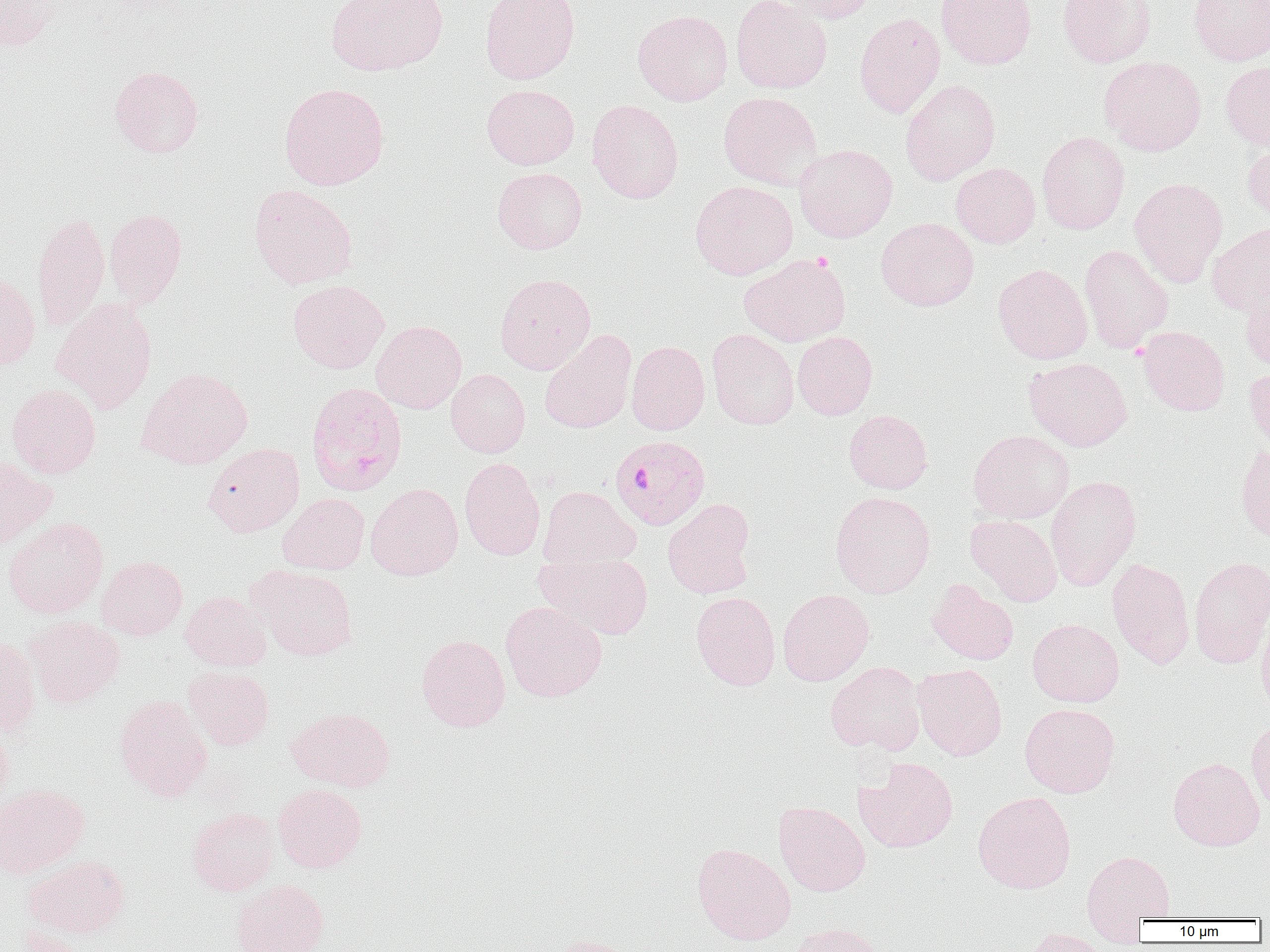 Approximate bounding boxes as named x1/y1/x2/y2 corners in pixels. Uninfected red blood cell locations: (x1=0, y1=0, x2=59, y2=51), (x1=325, y1=0, x2=448, y2=76), (x1=480, y1=0, x2=581, y2=85), (x1=731, y1=0, x2=832, y2=93), (x1=776, y1=0, x2=880, y2=23), (x1=936, y1=0, x2=1038, y2=69), (x1=1058, y1=0, x2=1156, y2=68), (x1=1188, y1=0, x2=1269, y2=66), (x1=633, y1=9, x2=733, y2=106), (x1=853, y1=12, x2=945, y2=118), (x1=1099, y1=56, x2=1207, y2=156), (x1=1221, y1=60, x2=1270, y2=152), (x1=109, y1=65, x2=204, y2=158), (x1=900, y1=80, x2=1001, y2=185), (x1=279, y1=82, x2=389, y2=190), (x1=481, y1=84, x2=579, y2=169), (x1=718, y1=92, x2=823, y2=191), (x1=587, y1=100, x2=683, y2=203), (x1=1037, y1=131, x2=1130, y2=234), (x1=1242, y1=139, x2=1270, y2=223), (x1=794, y1=144, x2=898, y2=242), (x1=950, y1=163, x2=1040, y2=248), (x1=492, y1=167, x2=587, y2=254), (x1=1129, y1=177, x2=1228, y2=287), (x1=690, y1=180, x2=798, y2=280), (x1=248, y1=184, x2=358, y2=290), (x1=104, y1=208, x2=187, y2=306), (x1=32, y1=213, x2=110, y2=331), (x1=876, y1=217, x2=979, y2=311), (x1=1207, y1=222, x2=1270, y2=318), (x1=1079, y1=244, x2=1173, y2=354), (x1=739, y1=254, x2=851, y2=347), (x1=992, y1=264, x2=1092, y2=364), (x1=0, y1=271, x2=40, y2=370), (x1=495, y1=273, x2=596, y2=374), (x1=287, y1=280, x2=389, y2=373), (x1=1240, y1=286, x2=1270, y2=373), (x1=52, y1=299, x2=157, y2=414), (x1=371, y1=321, x2=467, y2=414), (x1=1137, y1=326, x2=1230, y2=415), (x1=707, y1=328, x2=799, y2=430), (x1=539, y1=330, x2=637, y2=433), (x1=792, y1=331, x2=878, y2=420), (x1=626, y1=341, x2=710, y2=435), (x1=1024, y1=357, x2=1132, y2=451), (x1=1244, y1=363, x2=1270, y2=456), (x1=137, y1=367, x2=252, y2=469), (x1=446, y1=369, x2=531, y2=458), (x1=6, y1=383, x2=101, y2=478), (x1=843, y1=410, x2=933, y2=493), (x1=968, y1=430, x2=1074, y2=524), (x1=202, y1=443, x2=304, y2=537), (x1=1235, y1=443, x2=1270, y2=545), (x1=0, y1=455, x2=57, y2=550), (x1=459, y1=457, x2=546, y2=560), (x1=1045, y1=475, x2=1142, y2=592), (x1=366, y1=483, x2=463, y2=581), (x1=537, y1=485, x2=641, y2=570), (x1=830, y1=490, x2=935, y2=598), (x1=278, y1=493, x2=369, y2=574), (x1=663, y1=499, x2=757, y2=599), (x1=965, y1=514, x2=1062, y2=606), (x1=3, y1=517, x2=108, y2=618), (x1=536, y1=551, x2=653, y2=640), (x1=96, y1=556, x2=187, y2=641), (x1=1189, y1=556, x2=1270, y2=669), (x1=1107, y1=558, x2=1195, y2=669), (x1=250, y1=565, x2=358, y2=661), (x1=927, y1=579, x2=1019, y2=665), (x1=777, y1=589, x2=875, y2=686), (x1=180, y1=591, x2=271, y2=672), (x1=691, y1=591, x2=780, y2=691), (x1=500, y1=601, x2=607, y2=702), (x1=1256, y1=612, x2=1270, y2=717), (x1=24, y1=616, x2=124, y2=709), (x1=1027, y1=619, x2=1124, y2=707), (x1=417, y1=634, x2=510, y2=731), (x1=0, y1=637, x2=41, y2=736), (x1=825, y1=661, x2=926, y2=755), (x1=912, y1=663, x2=1007, y2=760), (x1=183, y1=666, x2=274, y2=750), (x1=113, y1=695, x2=212, y2=801), (x1=1020, y1=703, x2=1120, y2=798), (x1=286, y1=707, x2=395, y2=791), (x1=1246, y1=716, x2=1270, y2=816), (x1=0, y1=721, x2=13, y2=810), (x1=854, y1=757, x2=958, y2=854), (x1=1168, y1=757, x2=1265, y2=851), (x1=273, y1=783, x2=366, y2=872), (x1=0, y1=784, x2=88, y2=878), (x1=972, y1=791, x2=1076, y2=894), (x1=773, y1=800, x2=871, y2=896), (x1=187, y1=807, x2=279, y2=896), (x1=691, y1=842, x2=796, y2=945), (x1=1081, y1=849, x2=1175, y2=931), (x1=23, y1=855, x2=129, y2=939), (x1=231, y1=879, x2=329, y2=952), (x1=788, y1=922, x2=886, y2=952), (x1=16, y1=925, x2=88, y2=952), (x1=1022, y1=928, x2=1112, y2=952), (x1=544, y1=935, x2=641, y2=952). Plasmodium falciparum-infected red blood cell locations: (x1=305, y1=382, x2=408, y2=497), (x1=610, y1=434, x2=711, y2=530). Slide-level diagnosis: Plasmodium falciparum. Light microscopy. Thin blood smear. Image is 1270×952 pixels. 1000x magnification. One field of a larger specimen.